Describe the morphology of the erythrocytes.
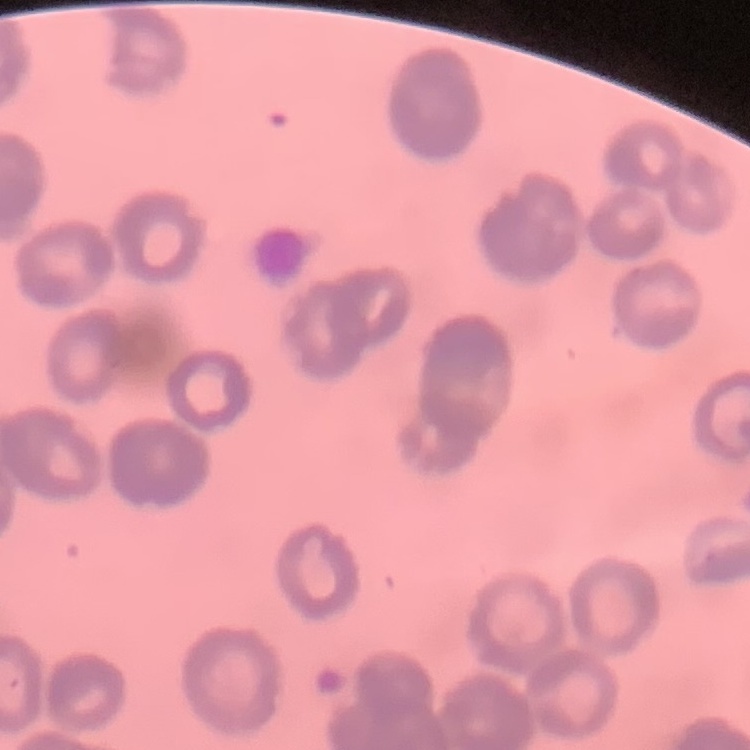
They show rouleaux formation.

One tile cut from a larger photomicrograph. Field's or Giemsa stain. Thin blood smear.